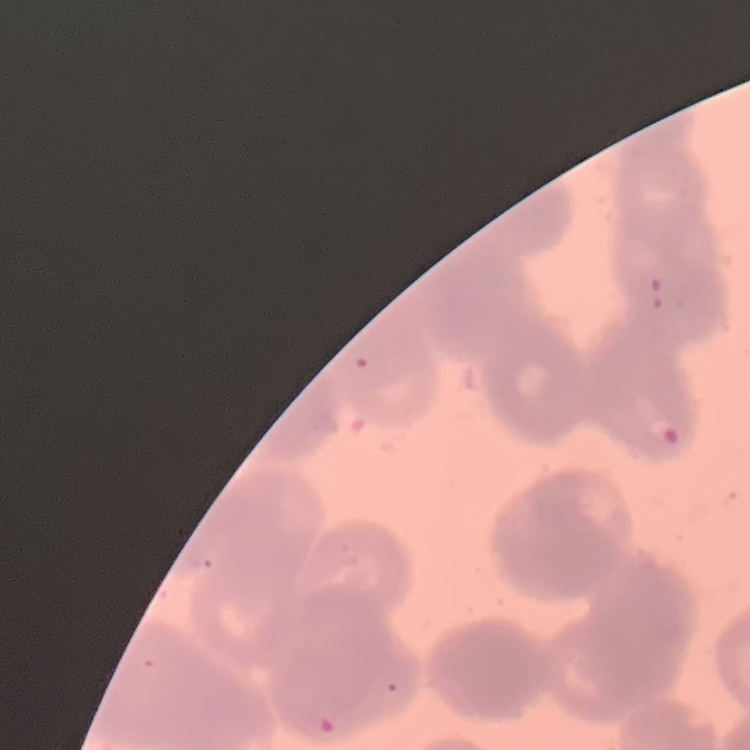
Summary:
  - Red blood cell morphology: rouleaux formation
  - Stain: Field's or Giemsa
  - Image type: one tile cut from a larger photomicrograph
  - Preparation: thin blood film